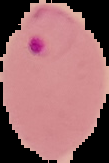

preparation = thin blood smear
image size = 109×163 pixels
image type = segmented cell region with the area outside set to black
result = malaria parasites detected